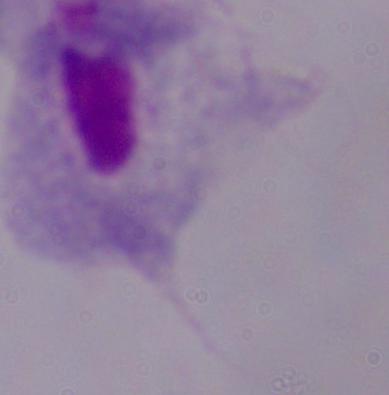

Summary:
  - Modality: photomicrograph
  - Identification: trichomonad
  - Magnification: 1000x